State which cell type is depicted.
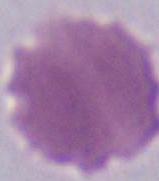
This is an erythrocyte.

1000x magnification. Photomicrograph.